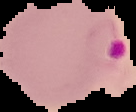 From a thin blood smear. Image is 136×112 pixels. Result: malaria parasites identified. The area outside the segmented cell region is set to black.